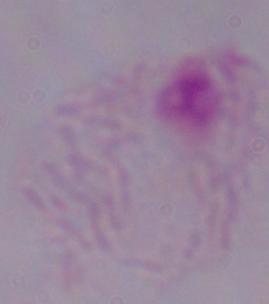
magnification = 1000x
modality = photomicrograph
identification = trichomonad